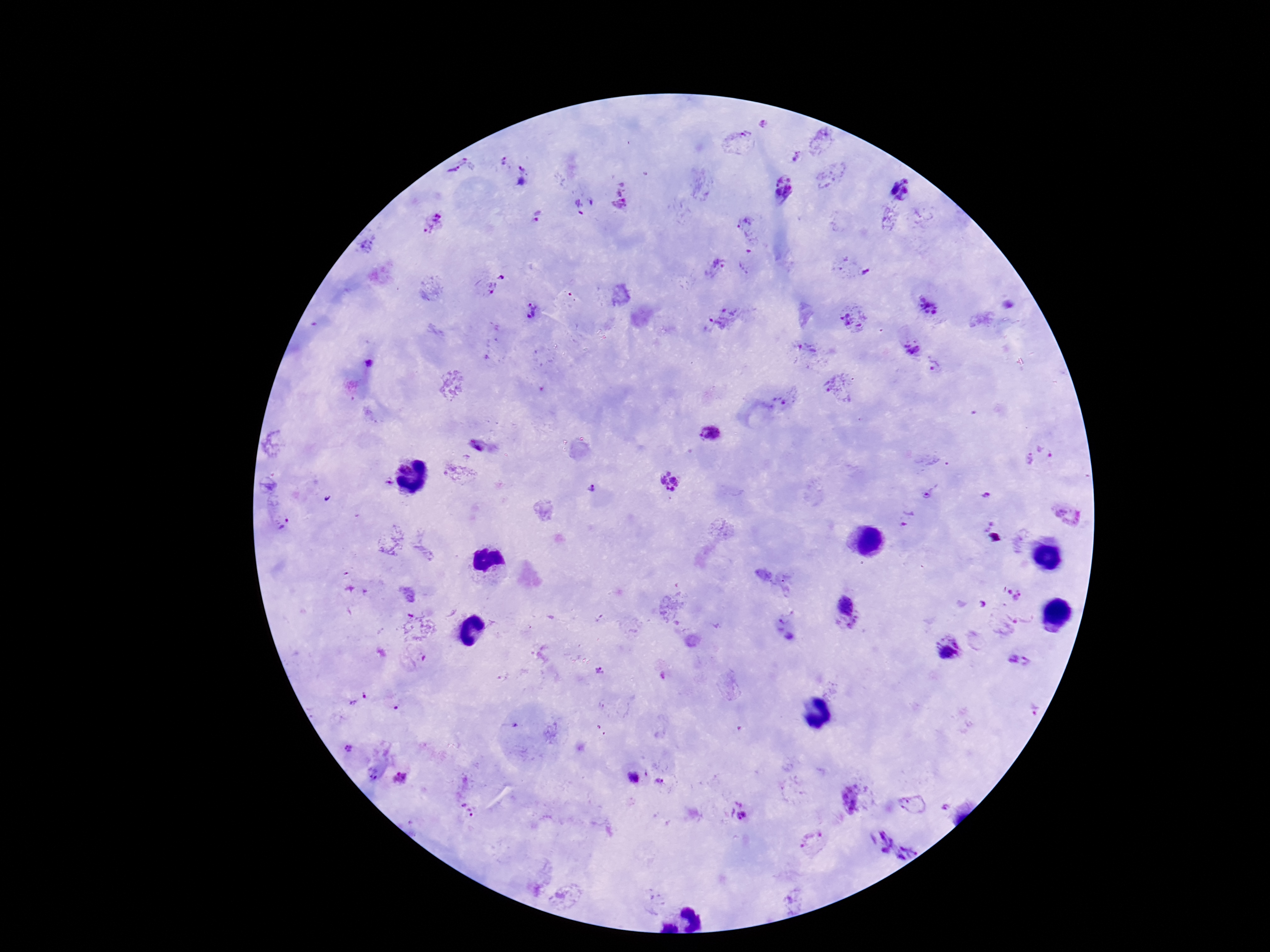

Approximate object centers, in pixels from the top-left corner.
Summary:
  - Plasmodium parasite locations: (x=741, y=140), (x=794, y=157), (x=504, y=165), (x=456, y=169), (x=529, y=177), (x=783, y=187), (x=898, y=189), (x=621, y=205), (x=539, y=216), (x=435, y=223), (x=745, y=226), (x=717, y=268), (x=864, y=272), (x=504, y=276), (x=489, y=287), (x=926, y=305), (x=532, y=311), (x=723, y=319), (x=854, y=319), (x=912, y=346), (x=807, y=349), (x=370, y=363), (x=936, y=367), (x=837, y=387), (x=788, y=398), (x=709, y=435), (x=1050, y=445), (x=478, y=446), (x=1027, y=459), (x=387, y=480), (x=666, y=484), (x=591, y=488), (x=984, y=495), (x=925, y=497), (x=905, y=517), (x=283, y=522), (x=1011, y=590), (x=851, y=612), (x=786, y=633), (x=947, y=646), (x=1016, y=658), (x=600, y=669), (x=359, y=700), (x=348, y=751), (x=632, y=775), (x=403, y=778), (x=660, y=779), (x=855, y=798), (x=947, y=808), (x=468, y=810), (x=738, y=811), (x=876, y=840), (x=909, y=852)
  - Preparation: thick peripheral-blood smear
  - Capture: smartphone camera through the microscope eyepiece
  - Patient malaria status: positive
  - Magnification: 100x
  - Field of view: one from this slide
  - Stain: Giemsa
  - Image size: 1270×952 pixels